Locate every blood parasite and identify its species.
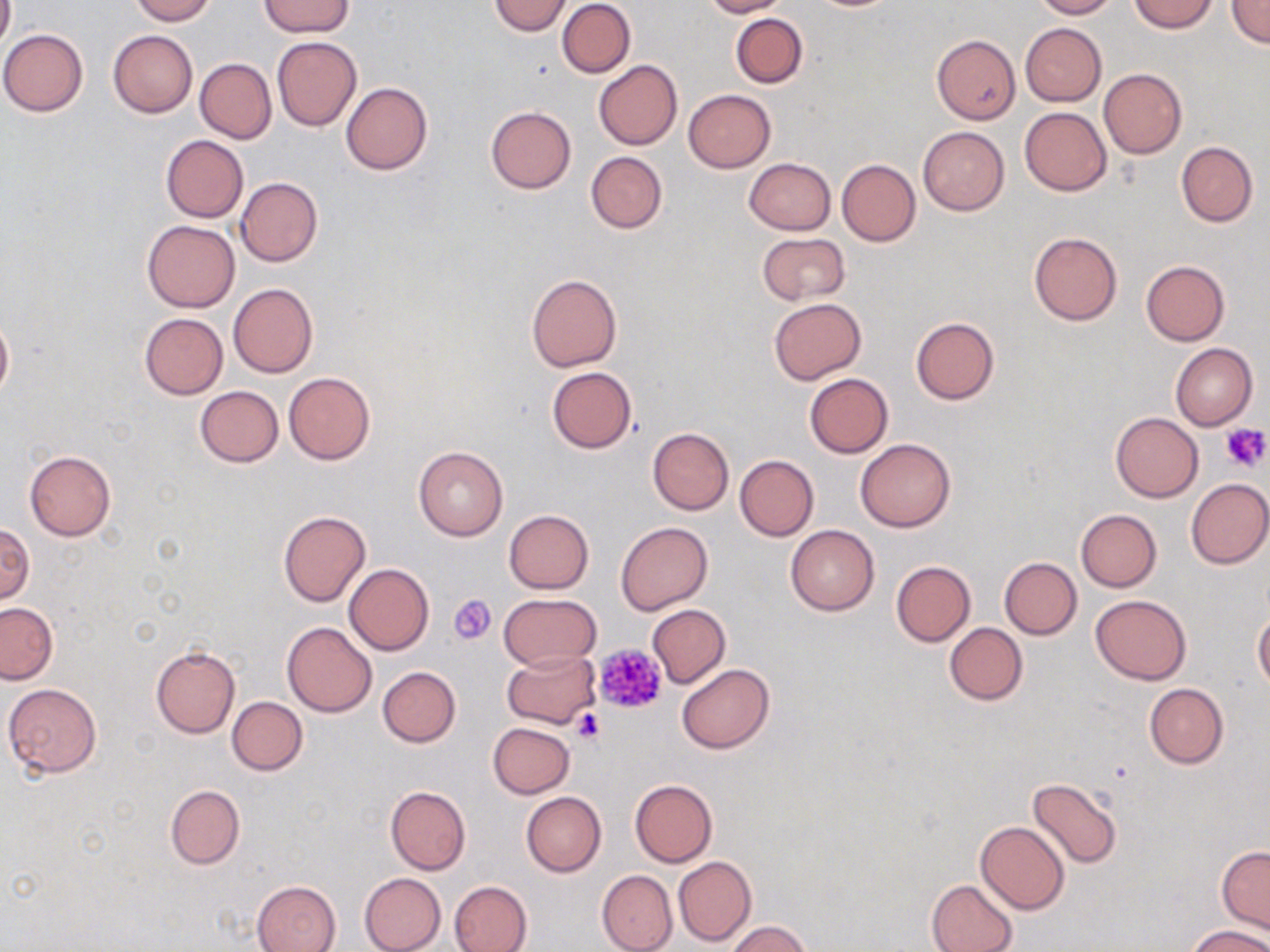
No blood parasites seen.

Summary:
  - Coordinate format: approximate bounding boxes as [x1, y1, x2, y2] in pixels
  - Platelet locations: [1222, 423, 1269, 475], [448, 594, 496, 645], [593, 643, 669, 715], [570, 708, 606, 744]
  - Uninfected red blood cell locations: [0, 0, 14, 53], [129, 0, 215, 24], [487, 0, 574, 35], [557, 0, 636, 78], [702, 0, 786, 17], [1031, 0, 1118, 19], [1130, 0, 1218, 33], [1226, 0, 1270, 48], [260, 2, 351, 35], [731, 13, 807, 88], [1021, 23, 1106, 105], [0, 29, 87, 117], [108, 29, 198, 118], [272, 36, 362, 131], [932, 36, 1020, 124], [195, 58, 275, 143], [594, 60, 682, 150], [1099, 68, 1187, 158], [341, 82, 432, 175], [683, 89, 775, 172], [485, 106, 575, 194], [1019, 107, 1113, 196], [918, 127, 1009, 215], [161, 135, 248, 222], [1176, 141, 1258, 226], [585, 151, 667, 234], [743, 158, 836, 234], [836, 159, 920, 246], [235, 177, 323, 266], [142, 220, 240, 312], [757, 232, 850, 305], [1028, 232, 1123, 326], [1141, 260, 1230, 346], [526, 273, 622, 373], [229, 282, 318, 378], [768, 298, 866, 384], [139, 313, 228, 398], [0, 314, 13, 404], [910, 317, 999, 405], [1170, 342, 1257, 430], [546, 366, 636, 453], [284, 371, 375, 465], [804, 373, 893, 458], [195, 386, 283, 468], [1110, 411, 1203, 502], [647, 428, 734, 515], [855, 438, 957, 532], [413, 445, 508, 540], [24, 450, 115, 540], [734, 455, 819, 541], [1185, 478, 1269, 568], [503, 509, 593, 593], [1075, 509, 1162, 591], [278, 511, 371, 606], [0, 522, 34, 606], [615, 522, 712, 614], [784, 525, 878, 615], [999, 557, 1082, 639], [891, 560, 975, 646], [344, 562, 433, 655], [498, 593, 600, 671], [1090, 593, 1192, 684], [0, 602, 57, 685], [648, 605, 730, 689], [1253, 612, 1270, 693], [283, 622, 376, 716], [944, 623, 1027, 705], [150, 646, 240, 738], [501, 649, 599, 728], [676, 663, 774, 754], [377, 666, 461, 747], [3, 683, 102, 777], [1144, 683, 1228, 768], [226, 696, 307, 775], [488, 722, 575, 798], [1027, 777, 1123, 868], [629, 778, 717, 866], [165, 784, 245, 869], [384, 785, 471, 875], [520, 791, 607, 877], [975, 821, 1070, 915], [1217, 845, 1270, 935], [673, 856, 756, 947], [597, 870, 677, 952], [359, 872, 446, 952], [926, 878, 1018, 952], [252, 880, 341, 952], [449, 880, 533, 952], [724, 921, 813, 952], [1186, 926, 1269, 952]
  - Slide-level diagnosis: negative for blood parasites
  - Image size: 1270×952 pixels
  - Stain: May-Grünwald-Giemsa
  - Modality: light microscopy
  - Magnification: 1000x
  - Preparation: thin blood film
  - Field of view: one of a larger specimen